State the blood parasite species.
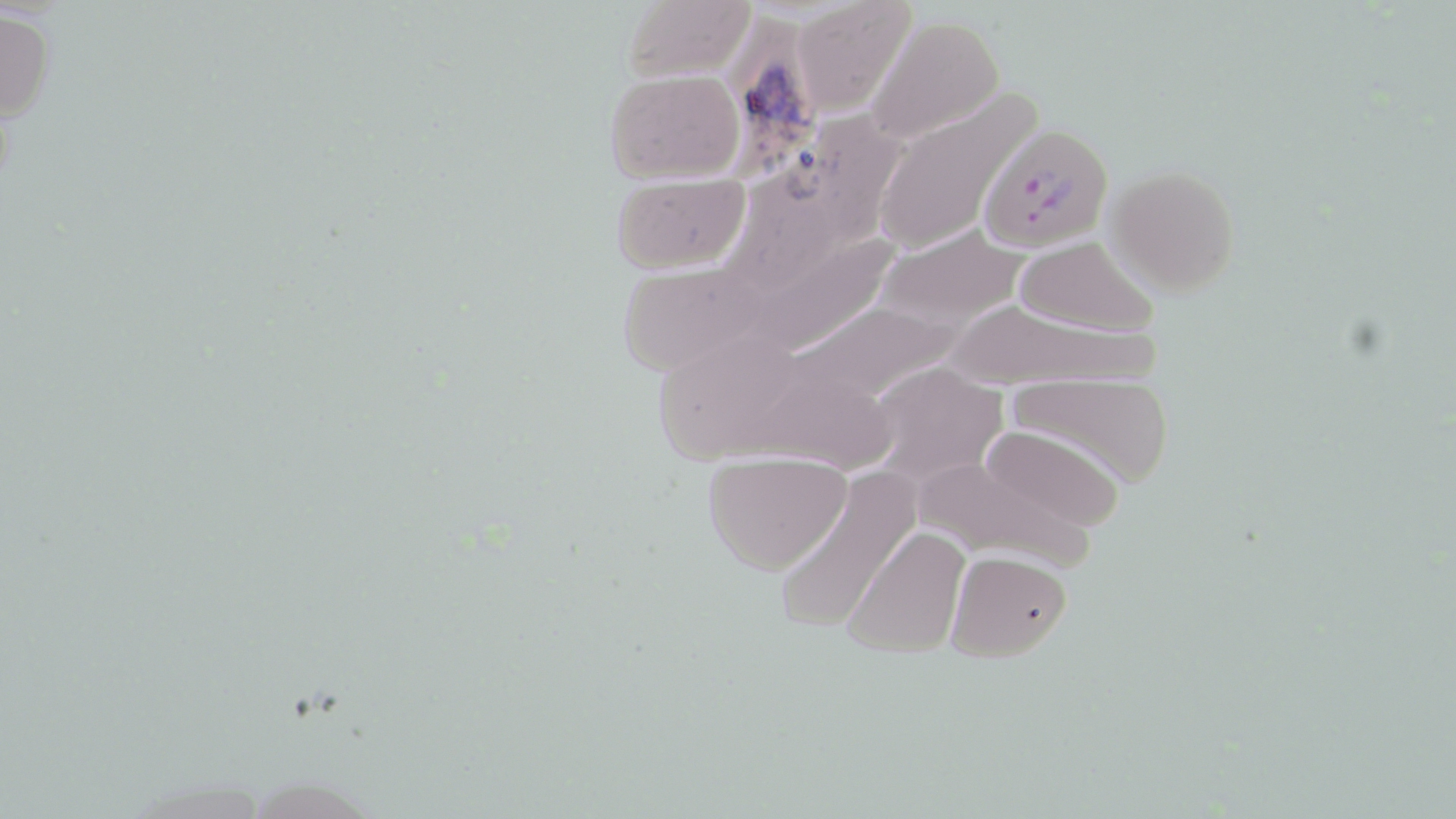
Plasmodium falciparum.

Summary:
  - Coordinate format: approximate bounding boxes as (x1,y1)-(x2,y2) corner pairs in pixels
  - Plasmodium falciparum-infected red blood cell locations: (980,121)-(1112,254)
  - Uninfected red blood cell locations: (790,0)-(916,116), (618,1)-(757,82), (0,10)-(56,123), (731,12)-(823,169), (868,15)-(1004,143), (603,68)-(746,184), (870,89)-(1041,257), (826,98)-(916,248), (743,143)-(849,300), (1105,163)-(1242,296), (609,174)-(751,274), (873,223)-(1032,329), (763,227)-(898,347), (1009,236)-(1161,338), (613,258)-(785,378), (802,290)-(964,412), (941,298)-(1156,392), (649,328)-(815,476), (866,364)-(1005,482), (761,369)-(910,471), (1004,370)-(1179,489), (976,424)-(1126,537), (912,448)-(1102,570), (702,453)-(851,575), (770,469)-(922,632), (841,525)-(973,660), (943,551)-(1071,663)
  - Magnification: 1000x
  - Stain: May-Grünwald-Giemsa
  - Field of view: one of a larger specimen
  - Preparation: thin blood film
  - Modality: light microscopy
  - Image size: 1456×819 pixels